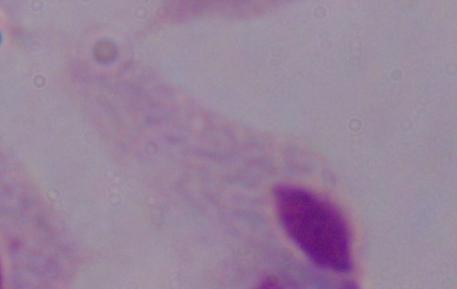
identification: trichomonad
modality: micrograph
magnification: 1000x